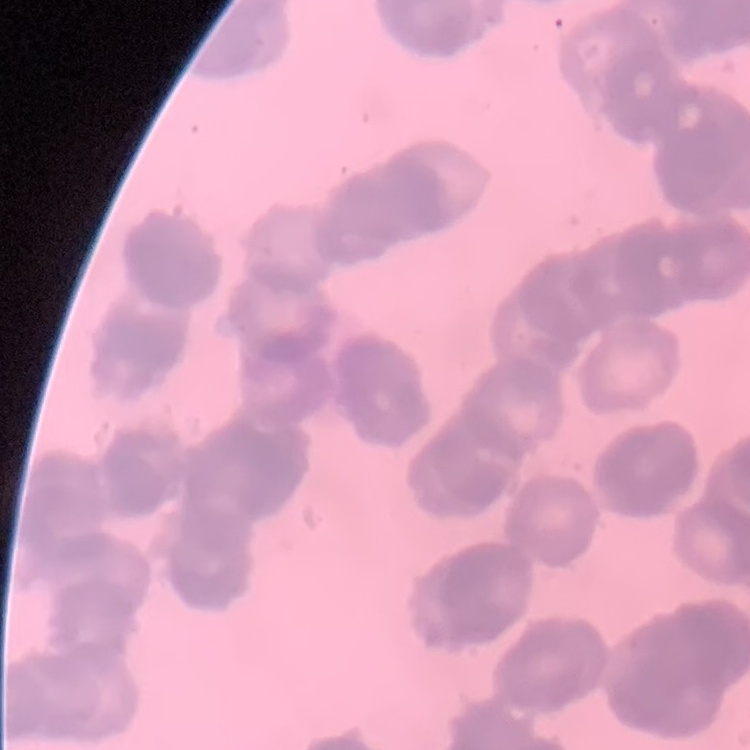
Summary:
  - Erythrocyte morphology: rouleaux formation
  - Image type: square crop of a larger photomicrograph
  - Preparation: thin blood film
  - Stain: Field's or Giemsa